Name the parasite shown.
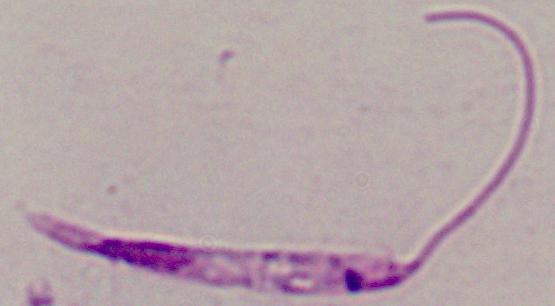
This is Leishmania.

Micrograph. Captured at 1000x magnification.